Outline each blood parasite and name the species.
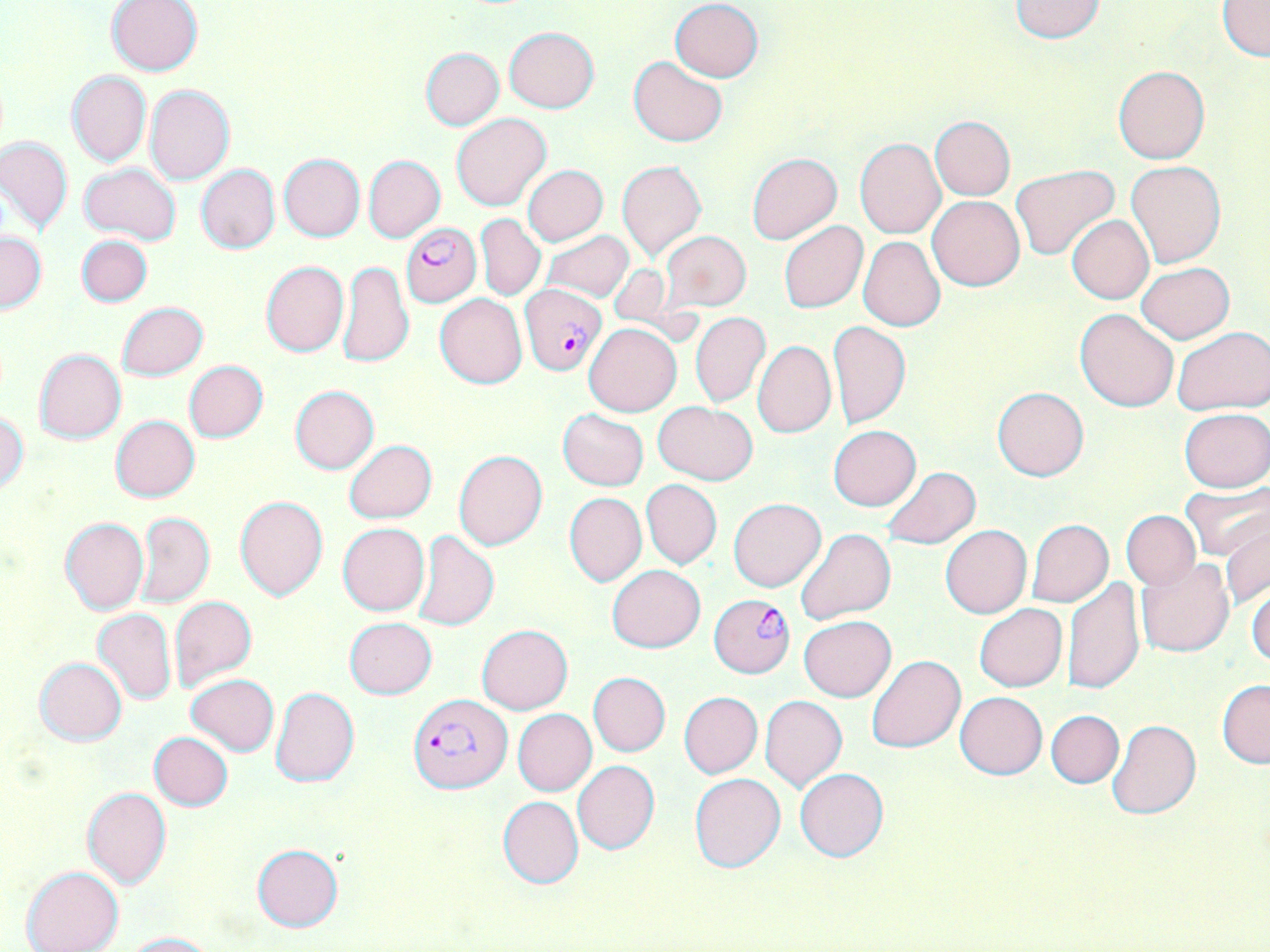

Approximate bounding boxes as [x1, y1, x2, y2] in pixels.
Plasmodium falciparum-infected red blood cells: [401, 224, 481, 307], [519, 284, 606, 375], [711, 594, 794, 675], [408, 694, 509, 794].
No Plasmodium ovale, Plasmodium malariae, Plasmodium vivax, Babesia divergens, or Trypanosoma brucei observed.

slide_level_diagnosis: Plasmodium falciparum
image_size: 1270×952 pixels
magnification: 1000x
modality: light microscopy
field_of_view: one of a larger specimen
preparation: thin blood film
uninfected_red_blood_cell_locations: 'approximate bounding boxes as [x1, y1, x2, y2] in pixels: [1008, 0, 1109, 43], [105, 1, 204, 76], [671, 1, 763, 82], [1217, 1, 1270, 59], [504, 26, 599, 113], [421, 48, 504, 130], [629, 56, 728, 147], [1113, 66, 1209, 164], [66, 71, 150, 166], [145, 84, 235, 185], [451, 113, 553, 211], [930, 117, 1015, 200], [0, 136, 72, 236], [855, 138, 945, 237], [746, 152, 843, 245], [278, 153, 365, 241], [363, 155, 445, 242], [616, 159, 706, 263], [1126, 160, 1226, 268], [79, 163, 181, 243], [196, 164, 280, 253], [522, 165, 608, 245], [1012, 165, 1119, 261], [928, 196, 1024, 290], [477, 214, 546, 301], [1066, 214, 1154, 304], [779, 221, 867, 314], [542, 230, 633, 301], [659, 231, 751, 313], [0, 232, 46, 313], [76, 235, 153, 307], [858, 237, 944, 330], [261, 261, 349, 357], [337, 261, 414, 368], [1137, 263, 1234, 343], [435, 294, 526, 388], [117, 302, 208, 380], [1075, 308, 1179, 412], [690, 312, 771, 408], [829, 319, 910, 429], [584, 322, 681, 416], [575, 325, 664, 493], [1171, 327, 1269, 416], [752, 340, 836, 439], [34, 348, 126, 444], [185, 361, 268, 443], [289, 385, 379, 473], [992, 386, 1088, 481], [653, 401, 759, 484], [1179, 408, 1269, 492], [558, 409, 649, 490], [1, 412, 28, 495], [110, 415, 199, 502], [828, 426, 921, 511], [344, 440, 437, 523], [453, 449, 548, 550], [881, 467, 981, 549], [641, 479, 722, 569], [1180, 482, 1270, 559], [565, 493, 647, 586], [234, 496, 328, 601], [728, 497, 826, 591], [1121, 510, 1201, 589], [136, 512, 214, 607], [1219, 516, 1270, 607], [60, 518, 148, 615], [1027, 519, 1113, 607], [338, 523, 429, 615], [940, 524, 1032, 618], [796, 528, 895, 624], [409, 530, 499, 631], [1136, 558, 1234, 658], [607, 565, 705, 652], [1063, 578, 1145, 697], [1247, 583, 1270, 668], [170, 596, 256, 693], [974, 603, 1066, 691], [93, 607, 177, 706], [799, 615, 896, 702], [345, 618, 437, 698], [477, 624, 572, 714], [866, 653, 965, 752], [35, 657, 127, 746], [588, 672, 670, 757], [187, 674, 280, 756], [1218, 680, 1269, 768], [270, 685, 360, 787], [679, 691, 762, 778], [955, 692, 1047, 779], [759, 695, 847, 791], [512, 709, 597, 796], [1046, 710, 1123, 787], [1106, 718, 1201, 819], [149, 732, 234, 811], [573, 761, 659, 854], [794, 768, 890, 861], [689, 772, 787, 873], [81, 787, 172, 889], [498, 797, 583, 888], [252, 844, 343, 932], [22, 866, 125, 952], [119, 930, 217, 951]'
stain: May-Grünwald-Giemsa